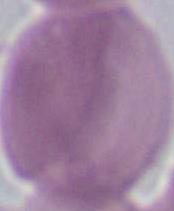

magnification = 1000x
identification = red blood cell
modality = photomicrograph